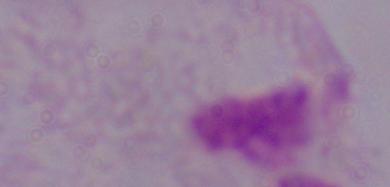
Summary:
  - Magnification: 1000x
  - Modality: photomicrograph
  - Identification: trichomonad